Assess the morphology of the red blood cells.
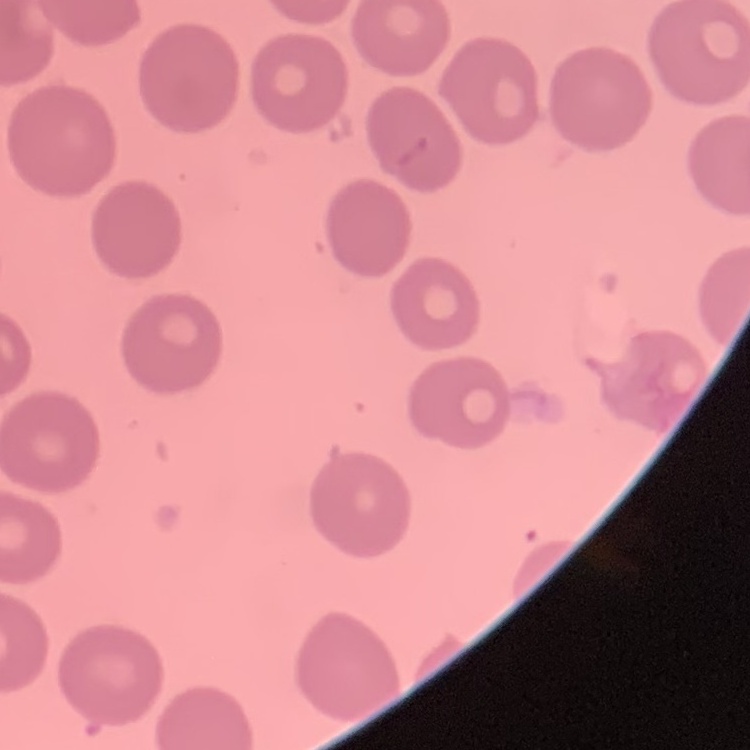
No rouleaux formation.

Summary:
  - Preparation: thin blood film
  - Stain: Field's or Giemsa
  - Image type: one tile cut from a larger photomicrograph